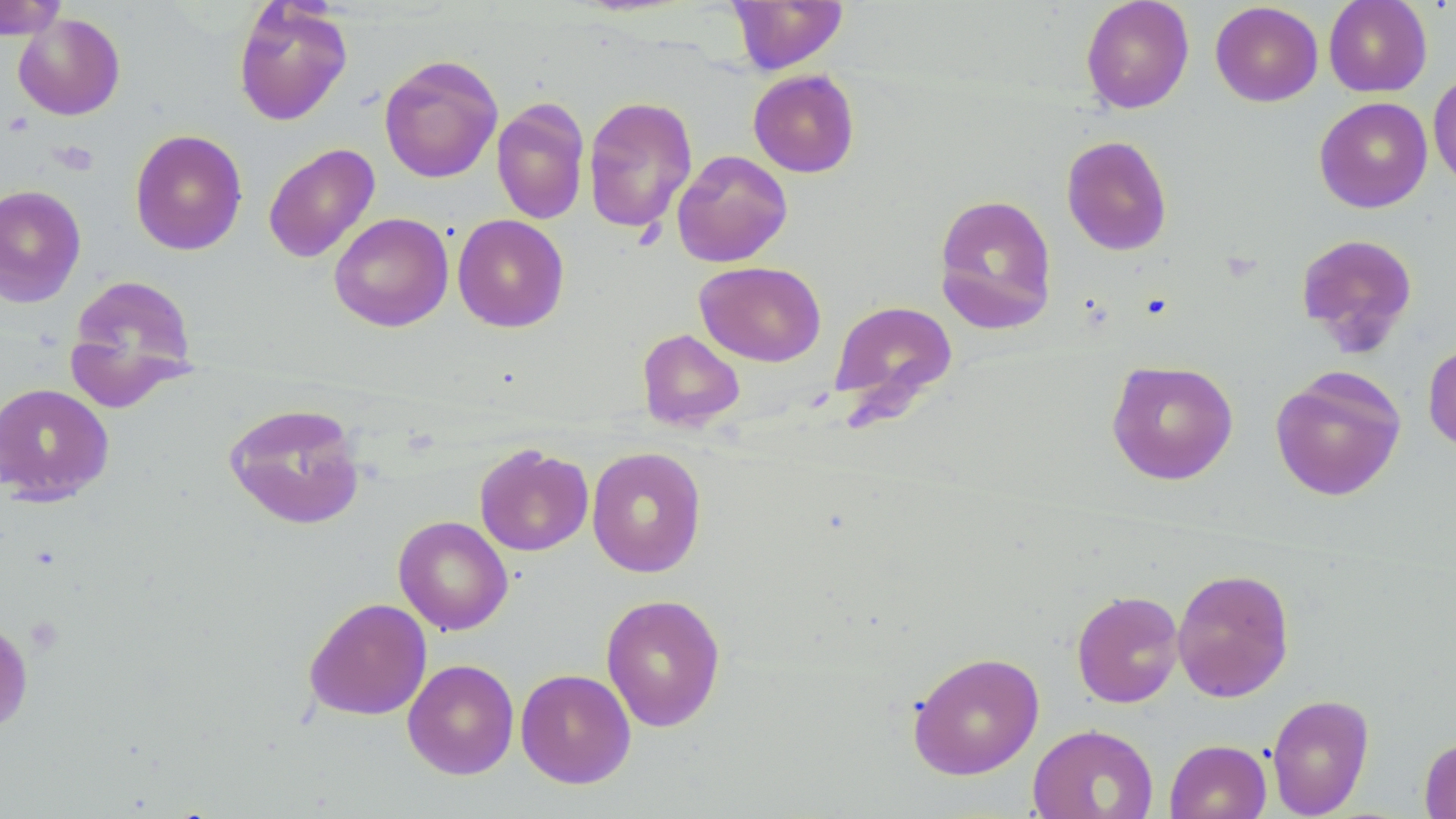
{
  "slide_level_diagnosis": "no evidence of blood parasites",
  "uninfected_red_blood_cell_locations": "approximate bounding boxes as [x1, y1, x2, y2] in pixels: [0, 0, 68, 40], [727, 0, 848, 74], [1080, 0, 1194, 113], [1324, 0, 1432, 97], [233, 2, 353, 126], [1210, 2, 1323, 106], [13, 12, 126, 120], [379, 54, 503, 183], [748, 69, 860, 178], [1428, 70, 1456, 193], [583, 95, 698, 234], [1314, 97, 1432, 213], [492, 98, 590, 225], [130, 129, 248, 255], [1061, 135, 1173, 256], [263, 142, 380, 263], [672, 150, 793, 268], [0, 184, 86, 309], [933, 193, 1058, 335], [329, 212, 454, 332], [452, 214, 570, 333], [1295, 232, 1419, 355], [695, 261, 826, 367], [65, 274, 199, 410], [829, 299, 958, 422], [637, 328, 744, 431], [1423, 339, 1456, 453], [1106, 359, 1239, 485], [1270, 366, 1406, 501], [0, 383, 114, 506], [224, 402, 366, 530], [474, 443, 594, 556], [586, 446, 707, 577], [393, 516, 513, 636], [1171, 567, 1295, 702], [1071, 590, 1184, 708], [600, 593, 726, 732], [304, 597, 432, 721], [0, 615, 34, 735], [907, 651, 1045, 779], [402, 658, 519, 780], [515, 668, 636, 789], [1266, 694, 1375, 818], [1027, 723, 1159, 819], [1419, 736, 1456, 819], [1164, 739, 1271, 819]",
  "stain": "May-Grünwald-Giemsa",
  "preparation": "thin blood smear",
  "image_size": "1456×819 pixels",
  "magnification": "1000x",
  "platelet_locations": "approximate bounding boxes as [x1, y1, x2, y2] in pixels: [52, 140, 98, 175]",
  "field_of_view": "single",
  "modality": "light microscopy"
}